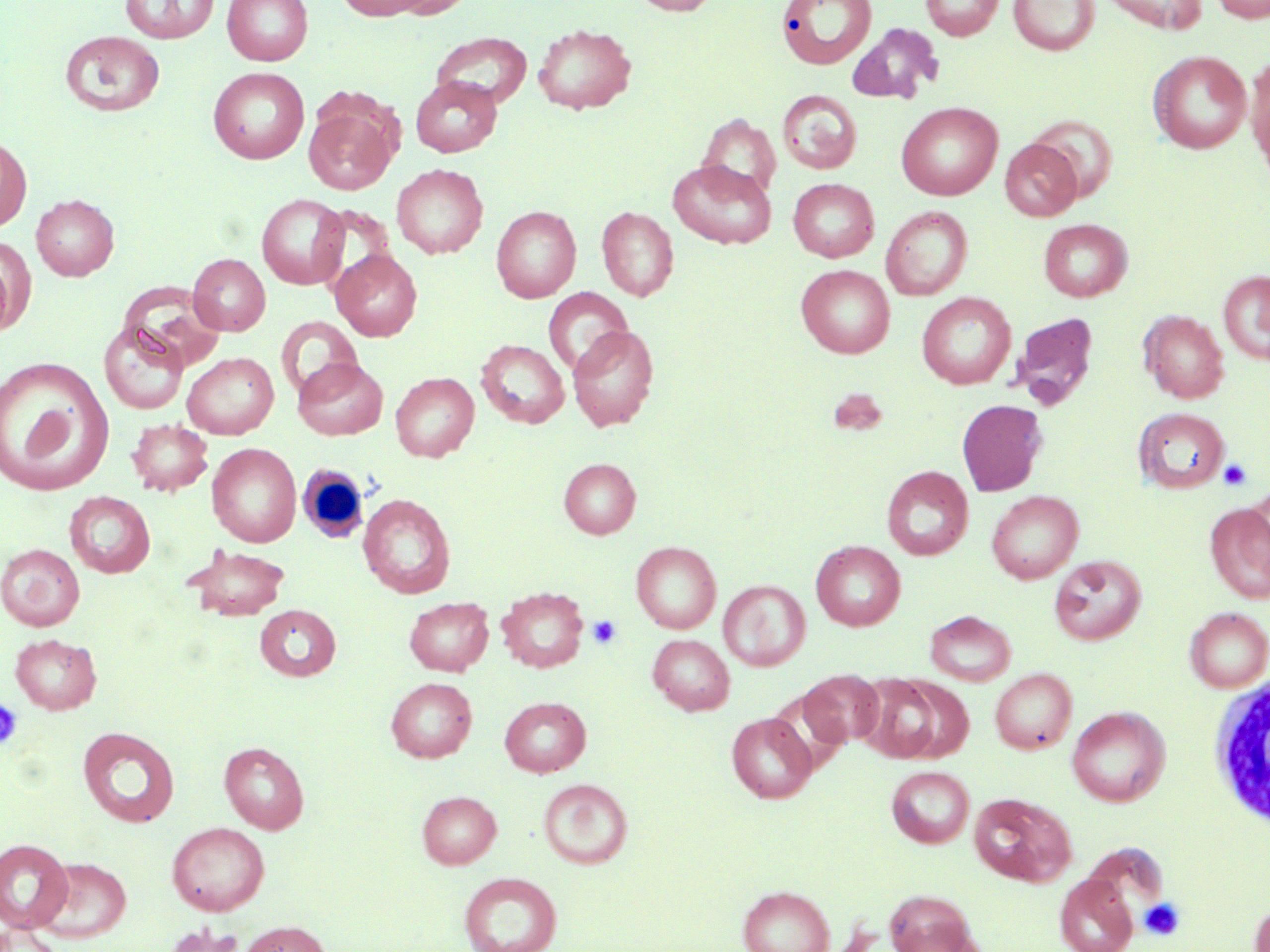

{
  "slide_level_diagnosis": "no evidence of blood parasites",
  "modality": "optical microscopy",
  "magnification": "1000x",
  "image_size": "1270×952 pixels",
  "uninfected_red_blood_cell_locations": "approximate bounding boxes as (x1, y1, x2, y2) in pixels: (119, 0, 220, 43), (222, 0, 313, 65), (335, 0, 432, 20), (388, 0, 476, 19), (630, 0, 720, 15), (776, 0, 878, 69), (920, 0, 1004, 41), (1009, 0, 1099, 55), (1099, 0, 1207, 33), (1210, 0, 1269, 23), (532, 23, 637, 114), (847, 23, 942, 104), (60, 31, 165, 117), (431, 32, 532, 110), (1149, 50, 1251, 154), (1249, 59, 1270, 179), (208, 67, 309, 164), (411, 76, 502, 157), (778, 89, 862, 174), (896, 102, 1002, 200), (304, 105, 396, 195), (698, 114, 781, 203), (1029, 116, 1119, 202), (0, 135, 32, 232), (1000, 139, 1082, 221), (668, 160, 776, 249), (392, 163, 488, 258), (788, 178, 879, 262), (31, 194, 119, 280), (257, 194, 349, 289), (491, 205, 581, 302), (597, 206, 678, 301), (882, 206, 972, 300), (1038, 218, 1132, 302), (0, 236, 35, 336), (331, 249, 422, 341), (188, 253, 270, 335), (796, 264, 895, 358), (1218, 270, 1270, 364), (120, 282, 226, 371), (544, 288, 633, 377), (916, 292, 1016, 389), (1139, 310, 1228, 403), (1008, 311, 1100, 411), (276, 316, 362, 403), (99, 321, 189, 415), (567, 325, 658, 432), (477, 339, 569, 428), (182, 352, 279, 439), (0, 356, 114, 496), (293, 357, 388, 440), (390, 372, 479, 461), (957, 400, 1046, 496), (1134, 408, 1230, 493), (127, 419, 212, 495), (207, 443, 301, 547), (559, 458, 640, 538), (882, 465, 973, 560), (1246, 485, 1270, 575), (987, 490, 1083, 583), (65, 491, 155, 578), (358, 494, 456, 598), (1205, 502, 1270, 604), (811, 540, 905, 631), (631, 541, 721, 633), (1, 544, 85, 630), (184, 544, 290, 622), (1050, 555, 1146, 645), (718, 580, 810, 671), (496, 587, 588, 672), (404, 597, 494, 676), (255, 605, 341, 681), (1184, 607, 1270, 692), (926, 610, 1016, 685), (9, 633, 102, 714), (648, 635, 734, 715), (990, 668, 1077, 754), (800, 669, 885, 746), (856, 673, 950, 763), (386, 677, 477, 762), (499, 696, 591, 777), (1067, 706, 1169, 806), (726, 712, 816, 803), (78, 726, 180, 827), (219, 741, 309, 833), (887, 766, 974, 848), (539, 779, 632, 869), (417, 791, 501, 868), (969, 792, 1076, 886), (167, 822, 270, 915), (0, 838, 73, 932), (34, 856, 132, 943), (459, 872, 562, 952), (1055, 873, 1138, 952), (738, 885, 835, 952), (883, 888, 980, 952), (1249, 900, 1270, 952), (237, 920, 332, 952), (162, 923, 246, 952), (0, 925, 66, 952)",
  "platelet_locations": "approximate bounding boxes as (x1, y1, x2, y2) in pixels: (1218, 458, 1252, 491), (587, 615, 622, 649), (0, 696, 24, 751), (1139, 898, 1185, 940)",
  "white_blood_cell_locations": "approximate bounding boxes as (x1, y1, x2, y2) in pixels: (296, 463, 371, 543), (1208, 674, 1269, 829)",
  "stain": "May-Grünwald-Giemsa",
  "preparation": "thin blood smear",
  "field_of_view": "single"
}